Identify the blood parasite species.
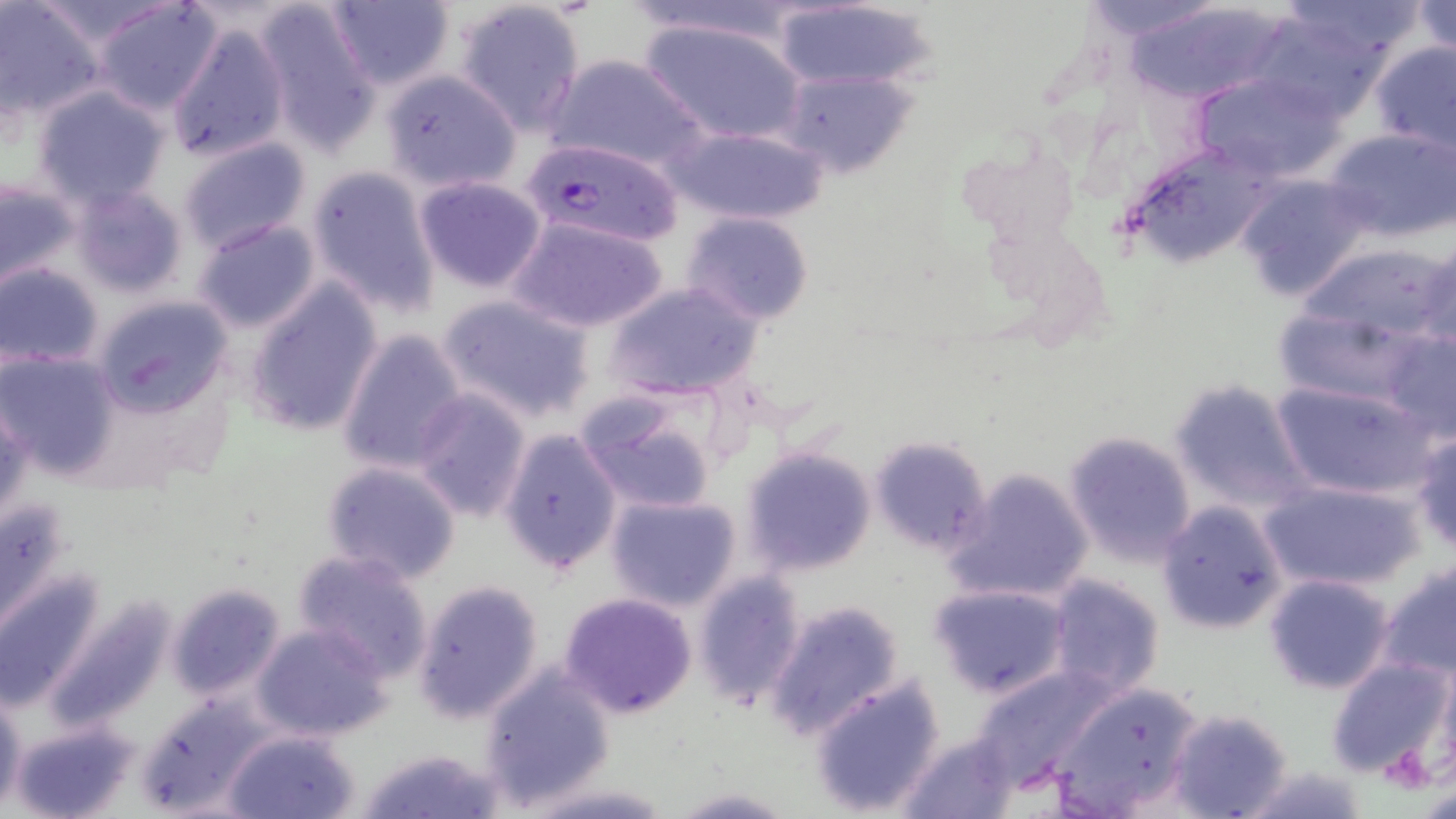

Plasmodium falciparum.

stain: May-Grünwald-Giemsa
plasmodium_falciparum_infected_red_blood_cell_locations: 'approximate bounding boxes as named x1/y1/x2/y2 corners in pixels: (x1=525, y1=139, x2=685, y2=248)'
uninfected_red_blood_cell_locations: 'approximate bounding boxes as named x1/y1/x2/y2 corners in pixels: (x1=0, y1=0, x2=100, y2=120), (x1=31, y1=0, x2=181, y2=47), (x1=324, y1=0, x2=456, y2=92), (x1=453, y1=0, x2=588, y2=135), (x1=621, y1=0, x2=816, y2=46), (x1=1077, y1=0, x2=1225, y2=43), (x1=1411, y1=0, x2=1456, y2=57), (x1=92, y1=1, x2=223, y2=115), (x1=252, y1=1, x2=381, y2=155), (x1=768, y1=2, x2=938, y2=93), (x1=1125, y1=2, x2=1292, y2=105), (x1=638, y1=17, x2=807, y2=145), (x1=167, y1=23, x2=289, y2=165), (x1=1369, y1=40, x2=1456, y2=154), (x1=545, y1=52, x2=706, y2=172), (x1=783, y1=69, x2=916, y2=179), (x1=1189, y1=69, x2=1341, y2=180), (x1=379, y1=70, x2=523, y2=193), (x1=32, y1=85, x2=171, y2=208), (x1=670, y1=123, x2=830, y2=227), (x1=1325, y1=126, x2=1456, y2=242), (x1=177, y1=136, x2=312, y2=252), (x1=1134, y1=153, x2=1275, y2=260), (x1=306, y1=166, x2=442, y2=316), (x1=1234, y1=175, x2=1368, y2=301), (x1=414, y1=176, x2=548, y2=293), (x1=0, y1=179, x2=80, y2=290), (x1=68, y1=184, x2=188, y2=298), (x1=681, y1=211, x2=815, y2=326), (x1=510, y1=214, x2=668, y2=333), (x1=190, y1=218, x2=323, y2=333), (x1=1416, y1=239, x2=1455, y2=360), (x1=1, y1=262, x2=105, y2=369), (x1=604, y1=282, x2=762, y2=403), (x1=243, y1=283, x2=383, y2=437), (x1=438, y1=294, x2=595, y2=423), (x1=94, y1=296, x2=233, y2=417), (x1=337, y1=327, x2=469, y2=475), (x1=1378, y1=327, x2=1456, y2=443), (x1=1, y1=349, x2=119, y2=477), (x1=1168, y1=381, x2=1307, y2=511), (x1=1270, y1=381, x2=1442, y2=503), (x1=408, y1=388, x2=533, y2=522), (x1=573, y1=389, x2=721, y2=513), (x1=1, y1=394, x2=33, y2=527), (x1=499, y1=427, x2=622, y2=575), (x1=1063, y1=430, x2=1198, y2=564), (x1=1412, y1=433, x2=1456, y2=554), (x1=869, y1=436, x2=991, y2=557), (x1=743, y1=446, x2=876, y2=575), (x1=321, y1=460, x2=462, y2=584), (x1=945, y1=467, x2=1095, y2=605), (x1=1259, y1=478, x2=1424, y2=594), (x1=2, y1=493, x2=73, y2=641), (x1=605, y1=493, x2=742, y2=612), (x1=1157, y1=501, x2=1288, y2=634), (x1=292, y1=549, x2=436, y2=683), (x1=1381, y1=559, x2=1456, y2=680), (x1=694, y1=570, x2=805, y2=711), (x1=2, y1=571, x2=104, y2=710), (x1=1264, y1=571, x2=1393, y2=694), (x1=1047, y1=573, x2=1165, y2=698), (x1=412, y1=579, x2=545, y2=724), (x1=167, y1=582, x2=287, y2=702), (x1=929, y1=583, x2=1068, y2=699), (x1=559, y1=592, x2=698, y2=719), (x1=764, y1=599, x2=905, y2=738), (x1=251, y1=622, x2=392, y2=741), (x1=1325, y1=655, x2=1452, y2=778), (x1=477, y1=665, x2=616, y2=811), (x1=970, y1=665, x2=1116, y2=792), (x1=809, y1=674, x2=947, y2=817), (x1=1051, y1=680, x2=1206, y2=816), (x1=0, y1=690, x2=25, y2=816), (x1=135, y1=694, x2=274, y2=816), (x1=1167, y1=707, x2=1294, y2=819), (x1=8, y1=719, x2=143, y2=819), (x1=226, y1=730, x2=362, y2=819), (x1=898, y1=732, x2=1019, y2=818), (x1=355, y1=746, x2=504, y2=819), (x1=1234, y1=764, x2=1368, y2=819), (x1=518, y1=782, x2=681, y2=817), (x1=669, y1=787, x2=794, y2=818)'
preparation: thin blood smear
magnification: 1000x
modality: optical microscopy
field_of_view: single
image_size: 1456×819 pixels